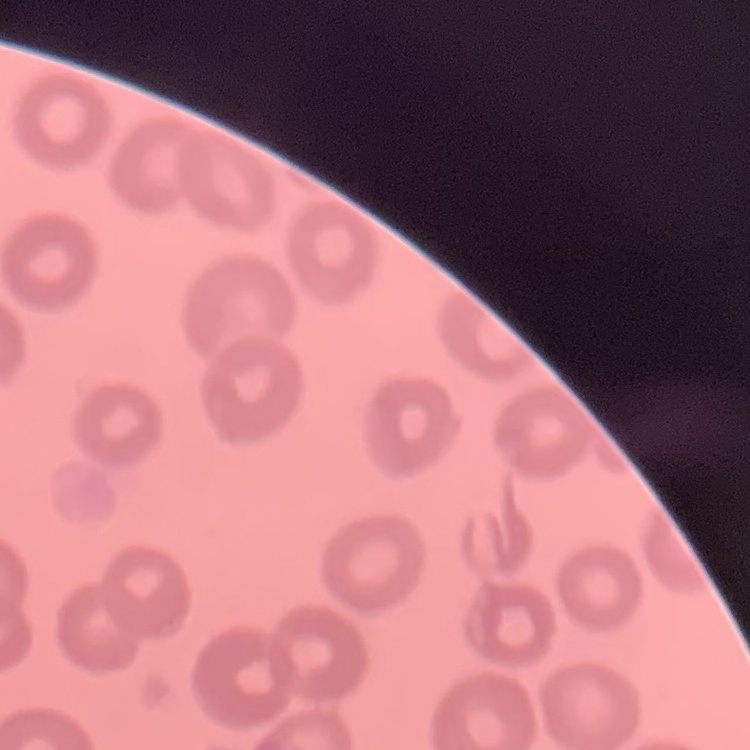

The red blood cells show no rouleaux formation. Square crop of a larger photomicrograph. Field's or Giemsa stain. Thin peripheral smear.